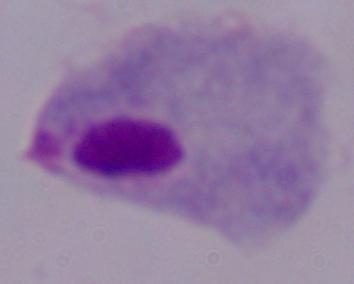

modality = micrograph
magnification = 1000x
identification = trichomonad